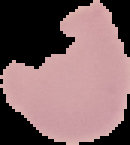

Segmented cell region on a black background. Malaria status: uninfected. Image is 130×145 pixels. From a thin blood smear.